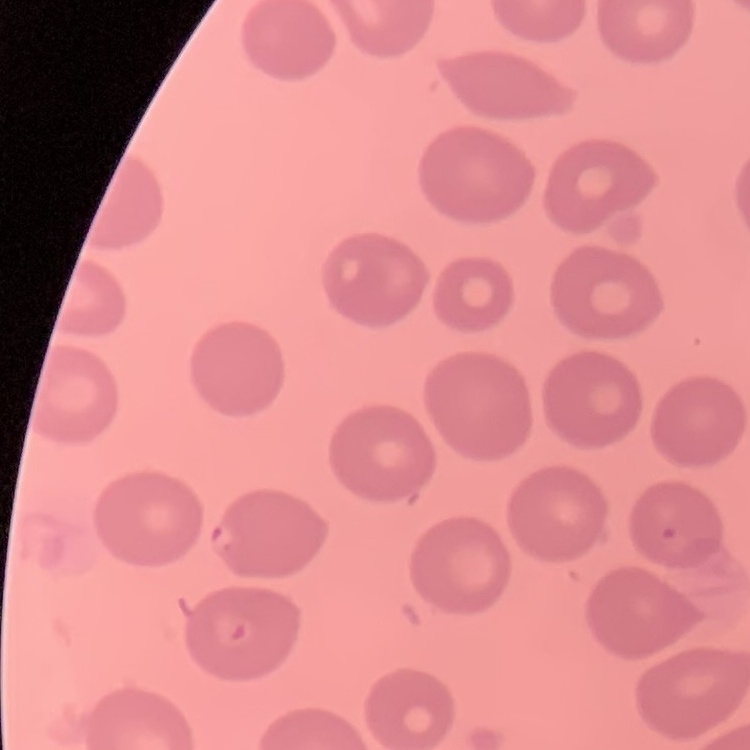
The erythrocytes exhibit no rouleaux formation. Thin blood film. Square crop of a larger photomicrograph. Field's or Giemsa stain.